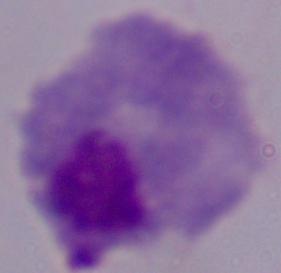

Summary:
  - Modality: micrograph
  - Identification: trichomonad
  - Magnification: 1000x